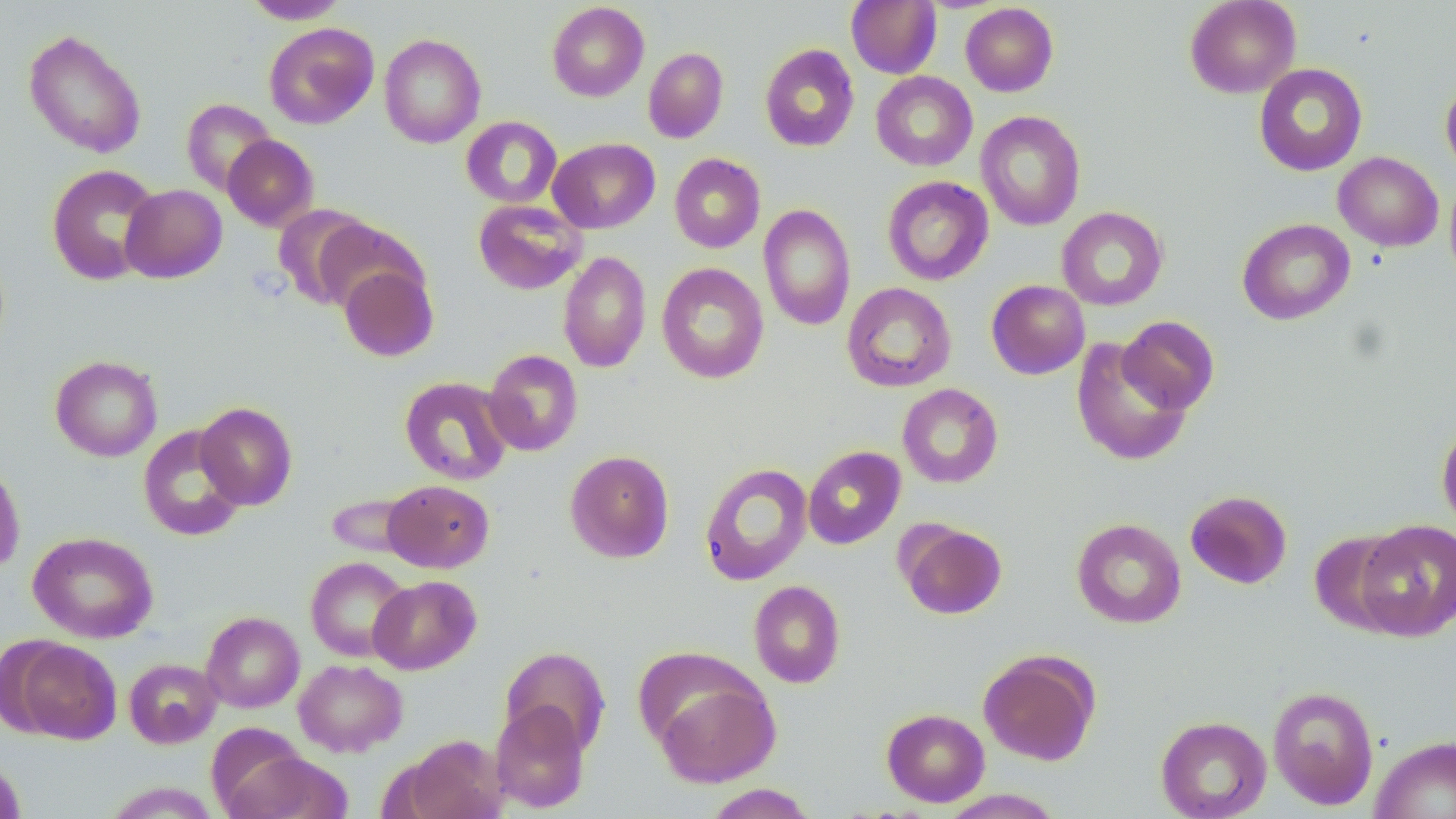
Summary:
  - Coordinate format: approximate bounding boxes as (x1, y1, x2, y2) in pixels
  - Uninfected red blood cell locations: (241, 0, 350, 24), (846, 0, 942, 79), (1184, 0, 1301, 98), (547, 2, 649, 102), (960, 3, 1059, 96), (264, 22, 379, 129), (23, 29, 147, 158), (379, 32, 486, 149), (759, 43, 859, 152), (643, 47, 729, 143), (1254, 62, 1368, 176), (871, 71, 977, 171), (1441, 78, 1456, 179), (181, 98, 276, 195), (975, 111, 1086, 231), (461, 116, 562, 208), (223, 134, 318, 231), (548, 138, 660, 233), (1334, 151, 1444, 251), (669, 153, 766, 253), (45, 163, 162, 285), (1445, 174, 1456, 288), (882, 176, 994, 285), (120, 184, 227, 283), (473, 199, 587, 295), (758, 203, 856, 331), (273, 204, 374, 309), (1057, 206, 1168, 311), (312, 217, 425, 314), (1237, 218, 1355, 325), (557, 251, 651, 372), (656, 262, 769, 384), (338, 263, 438, 362), (986, 280, 1090, 379), (842, 282, 956, 392), (1117, 315, 1220, 415), (1070, 338, 1192, 466), (482, 349, 583, 456), (50, 354, 163, 461), (399, 376, 514, 485), (897, 383, 1003, 488), (195, 402, 298, 509), (1437, 420, 1456, 532), (138, 425, 247, 541), (803, 446, 906, 549), (565, 450, 674, 563), (0, 462, 25, 575), (698, 462, 813, 586), (382, 479, 494, 573), (1185, 490, 1292, 589), (325, 491, 421, 559), (1072, 517, 1186, 628), (1354, 519, 1456, 640), (898, 521, 1007, 619), (1310, 529, 1412, 635), (28, 531, 158, 643), (306, 557, 412, 662), (368, 575, 481, 674), (749, 580, 845, 688), (201, 611, 304, 712), (11, 638, 122, 744), (500, 645, 611, 756), (978, 649, 1100, 765), (124, 657, 221, 749), (293, 658, 408, 757), (653, 678, 780, 788), (1267, 685, 1379, 810), (491, 700, 590, 813), (882, 708, 989, 807), (1156, 715, 1271, 819), (401, 734, 507, 819), (1370, 736, 1456, 819), (224, 750, 354, 819), (0, 756, 26, 819), (704, 784, 819, 818), (938, 789, 1064, 818)
  - Slide-level diagnosis: no evidence of blood parasites
  - Stain: May-Grünwald-Giemsa
  - Field of view: single
  - Modality: optical microscopy
  - Magnification: 1000x
  - Image size: 1456×819 pixels
  - Preparation: thin blood smear